Outline each uninfected red blood cell.
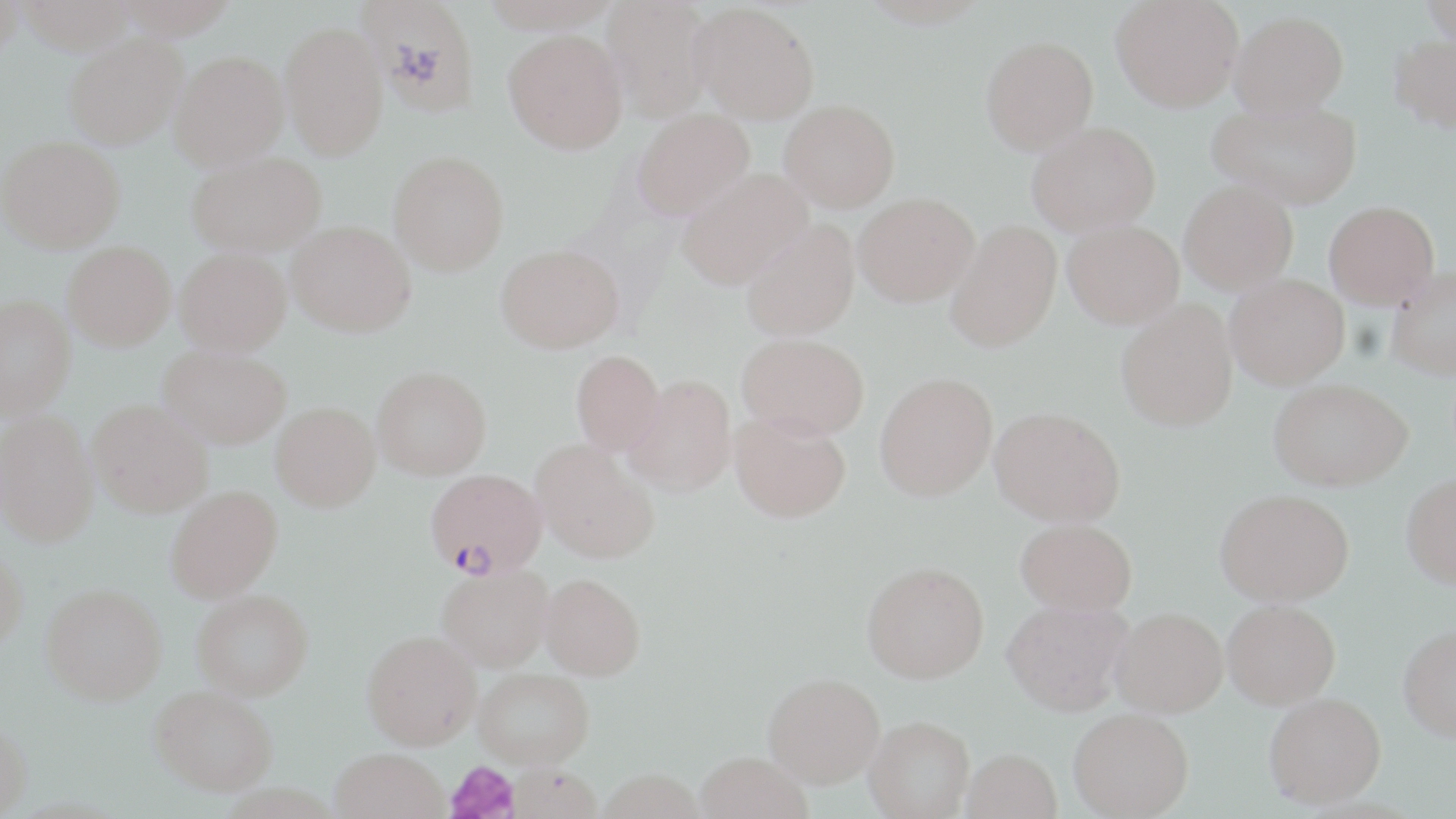

Approximate bounding boxes as (x1,y1)-(x2,y2) corner pairs in pixels.
Uninfected red blood cells: (0,0)-(24,60), (16,0)-(139,54), (112,0)-(240,39), (357,0)-(480,114), (601,0)-(717,121), (1111,0)-(1243,112), (1422,0)-(1456,48), (690,2)-(820,124), (1230,10)-(1349,117), (280,21)-(388,160), (503,29)-(627,153), (64,34)-(186,150), (1389,34)-(1456,134), (981,35)-(1098,154), (170,50)-(288,170), (1208,97)-(1363,209), (779,99)-(900,211), (631,107)-(755,220), (1027,121)-(1161,236), (0,136)-(125,252), (187,151)-(326,256), (388,151)-(509,275), (676,168)-(813,289), (1179,180)-(1299,294), (854,193)-(979,306), (1324,200)-(1440,308), (741,219)-(860,341), (946,219)-(1062,352), (1062,219)-(1185,328), (287,220)-(416,336), (63,240)-(176,350), (496,244)-(624,353), (174,248)-(292,355), (1387,266)-(1456,380), (1226,274)-(1350,389), (0,294)-(75,420), (1116,299)-(1238,431), (737,333)-(870,439), (159,346)-(291,448), (571,350)-(666,455), (372,366)-(491,479), (875,371)-(998,500), (625,373)-(737,496), (1269,378)-(1412,490), (88,399)-(213,517), (270,401)-(380,511), (990,406)-(1126,526), (0,411)-(98,546), (730,411)-(851,522), (532,439)-(659,563), (1401,472)-(1456,588), (165,485)-(283,603), (1216,488)-(1355,606), (1016,518)-(1137,614), (0,545)-(28,652), (861,561)-(989,683), (437,564)-(553,671), (540,573)-(645,680), (41,583)-(167,705), (192,589)-(313,699), (1002,599)-(1134,715), (1222,599)-(1340,708), (1111,607)-(1228,717), (1398,624)-(1456,742), (363,630)-(481,749), (474,668)-(594,767), (764,672)-(885,787), (150,685)-(278,795), (1264,692)-(1386,807), (1069,708)-(1194,818), (864,715)-(974,818), (0,721)-(32,818), (330,748)-(449,819), (962,748)-(1062,819), (694,752)-(812,819), (504,763)-(602,819), (597,769)-(704,819).

Plasmodium falciparum-infected red blood cell locations = approximate bounding boxes as (x1,y1)-(x2,y2) corner pairs in pixels: (426,469)-(545,576)
slide-level diagnosis = Plasmodium falciparum
image size = 1456×819 pixels
stain = May-Grünwald-Giemsa
modality = optical microscopy
field of view = one of a larger specimen
platelet locations = approximate bounding boxes as (x1,y1)-(x2,y2) corner pairs in pixels: (445,760)-(520,819)
magnification = 1000x
preparation = thin blood film